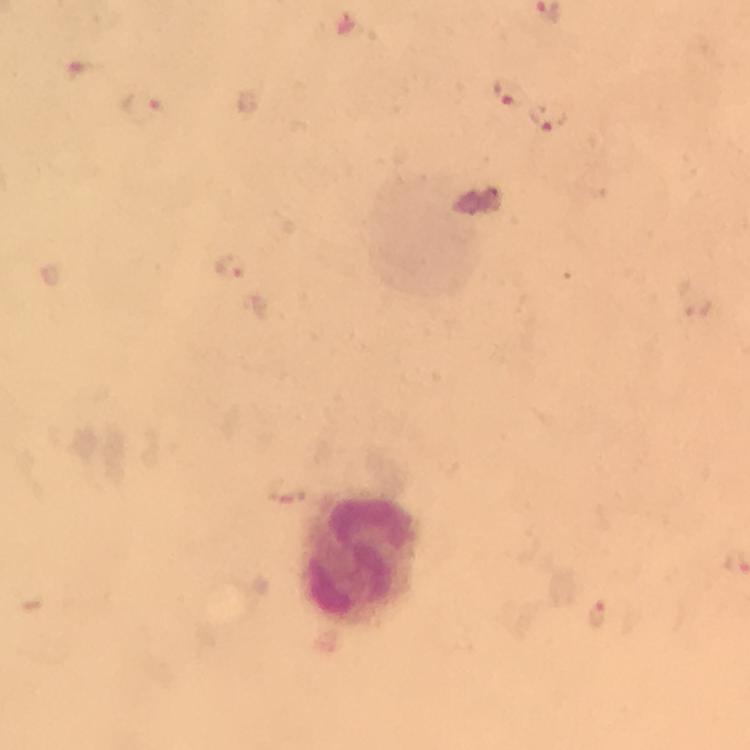 Approximate centers as (x, y) in pixels. Malaria parasite locations: (507, 93), (142, 106), (549, 119), (230, 265), (597, 613). Leukocyte locations: (356, 560). Immersion oil applied. From a malaria diagnostic workup. Thick blood film. Image is 750×750 pixels. 100x magnification. Photographed with a smartphone mounted on the microscope. Giemsa stain. A crop from one field of view.